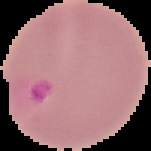
Summary:
  - Image type: segmented cell region with the area outside set to black
  - Preparation: thin blood smear
  - Malaria status: parasitized
  - Image size: 151×151 pixels